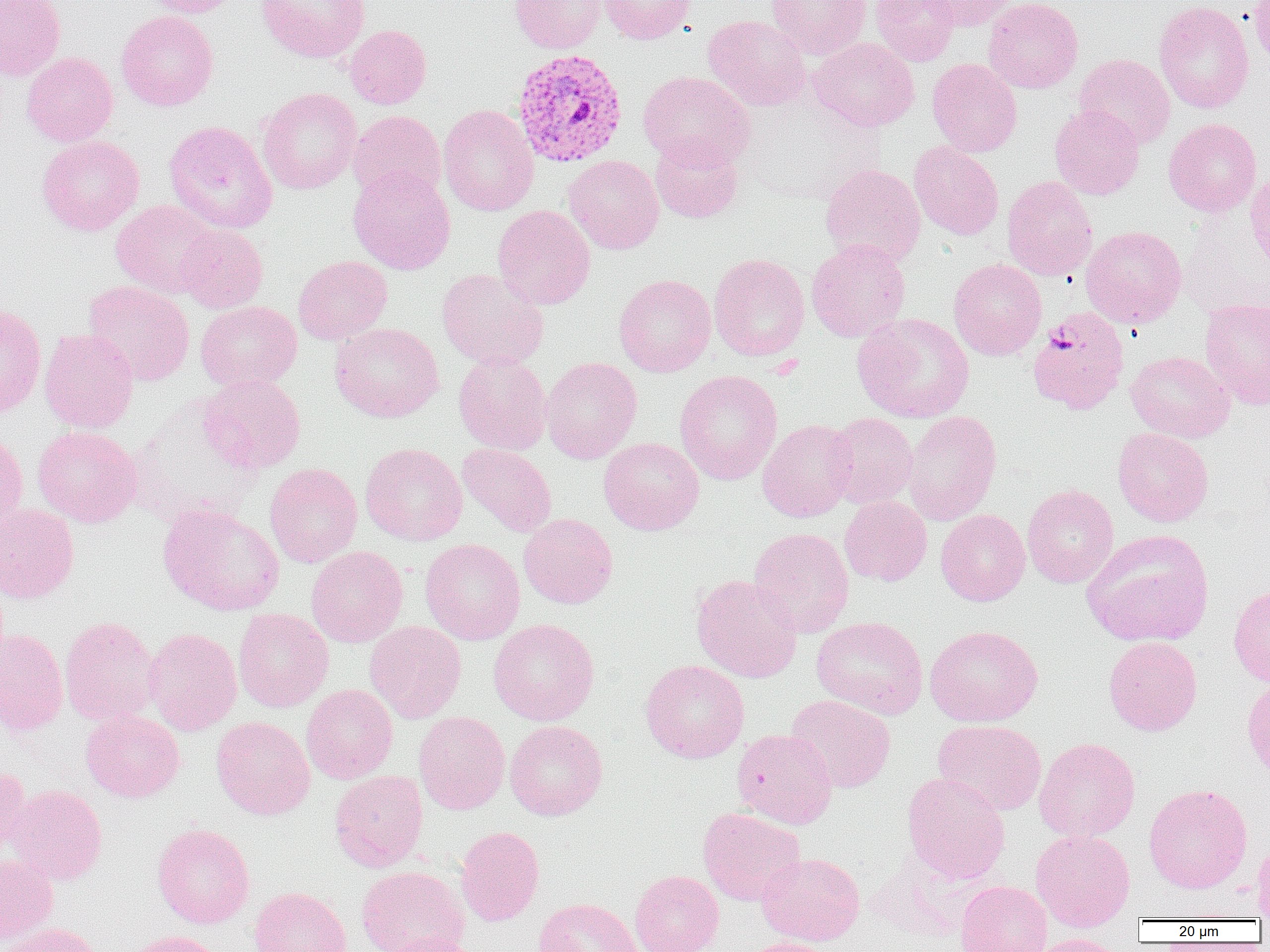

Summary:
  - Coordinate format: approximate bounding boxes as (x1,y1)-(x2,y2) corner pairs in pixels
  - Uninfected red blood cell locations: (0,0)-(65,81), (138,0)-(245,17), (256,0)-(370,63), (509,0)-(606,53), (599,0)-(697,44), (766,0)-(871,60), (870,0)-(960,66), (918,0)-(1014,30), (984,0)-(1083,94), (1249,0)-(1270,66), (1153,1)-(1254,113), (116,10)-(219,111), (703,15)-(810,111), (345,24)-(432,109), (808,37)-(920,131), (22,52)-(118,146), (1074,53)-(1175,150), (927,58)-(1022,158), (638,71)-(755,169), (257,87)-(361,194), (437,104)-(539,217), (1050,105)-(1146,199), (348,110)-(446,201), (1164,118)-(1262,217), (163,120)-(278,234), (36,134)-(144,235), (650,134)-(744,223), (909,142)-(1004,240), (564,155)-(663,254), (820,164)-(926,268), (348,166)-(456,275), (1245,169)-(1270,273), (1002,176)-(1097,280), (111,199)-(221,297), (492,205)-(595,310), (176,225)-(268,313), (1081,225)-(1187,328), (806,239)-(911,342), (709,253)-(810,361), (293,255)-(393,344), (948,258)-(1047,360), (437,269)-(549,370), (613,274)-(716,377), (83,280)-(195,386), (1200,298)-(1270,410), (195,301)-(302,391), (0,304)-(46,418), (852,313)-(974,423), (329,322)-(444,423), (39,328)-(138,433), (1126,351)-(1235,442), (453,353)-(552,454), (541,357)-(642,464), (674,370)-(782,484), (200,375)-(306,474), (902,411)-(1002,525), (825,413)-(919,509), (757,418)-(857,522), (32,426)-(141,527), (1112,427)-(1214,527), (0,429)-(27,535), (598,437)-(704,535), (360,442)-(468,546), (458,443)-(556,537), (264,463)-(362,568), (1022,483)-(1119,588), (839,495)-(932,586), (0,503)-(79,604), (158,503)-(284,616), (936,509)-(1030,606), (519,513)-(618,609), (749,527)-(854,638), (1082,529)-(1214,647), (420,538)-(525,645), (306,546)-(408,647), (691,574)-(802,683), (1228,583)-(1270,688), (233,608)-(334,712), (59,616)-(160,727), (811,616)-(929,719), (488,618)-(600,725), (364,620)-(466,723), (925,624)-(1043,727), (144,627)-(242,735), (0,628)-(68,736), (1104,636)-(1202,735), (639,659)-(750,763), (1241,677)-(1270,782), (301,684)-(398,783), (786,694)-(896,792), (81,710)-(185,802), (413,711)-(510,814), (211,716)-(315,820), (933,719)-(1046,815), (505,720)-(608,820), (731,728)-(838,829), (1034,737)-(1141,841), (0,766)-(31,859), (329,770)-(428,871), (901,772)-(1010,884), (1143,783)-(1253,893), (6,784)-(108,884), (697,807)-(806,906), (152,823)-(255,928), (456,826)-(544,925), (1030,829)-(1136,931), (1252,836)-(1270,919), (756,852)-(865,946), (0,854)-(58,945), (355,865)-(469,952), (629,869)-(724,952), (955,880)-(1052,951), (249,886)-(352,952), (533,897)-(641,952), (1,922)-(102,952), (120,931)-(227,952), (384,934)-(483,952), (1027,934)-(1131,952), (737,938)-(840,952)
  - Plasmodium vivax-infected red blood cell locations: (511,48)-(629,168), (1028,308)-(1130,414)
  - Slide-level diagnosis: Plasmodium vivax
  - Magnification: 1000x
  - Modality: light microscopy
  - Preparation: thin blood film
  - Field of view: single
  - Image size: 1270×952 pixels